Name the parasite shown.
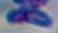
Toxoplasma gondii.

Summary:
  - Magnification: 1000x
  - Modality: micrograph